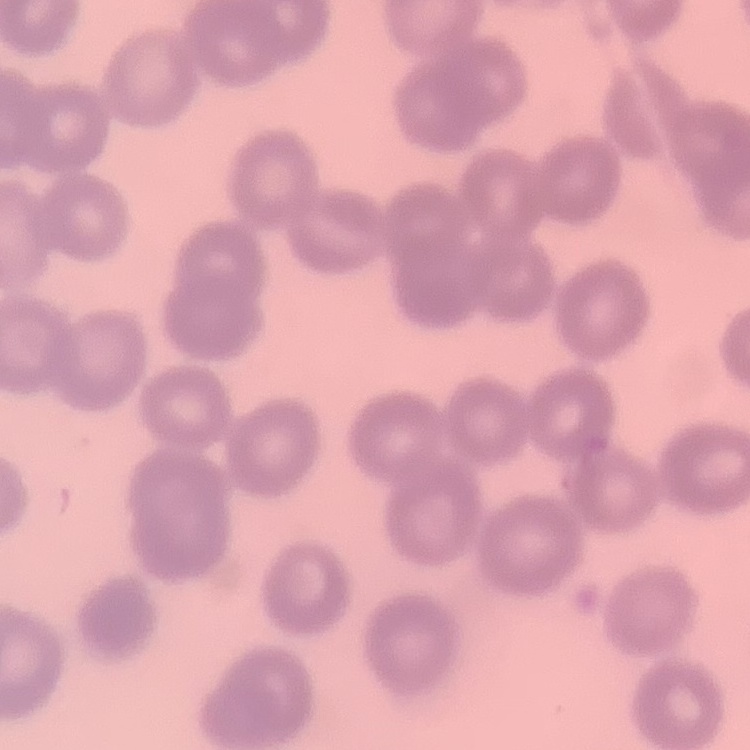 The erythrocytes show no rouleaux formation. One tile cut from a larger photomicrograph. Thin peripheral smear. Stained with either Field's or Giemsa.